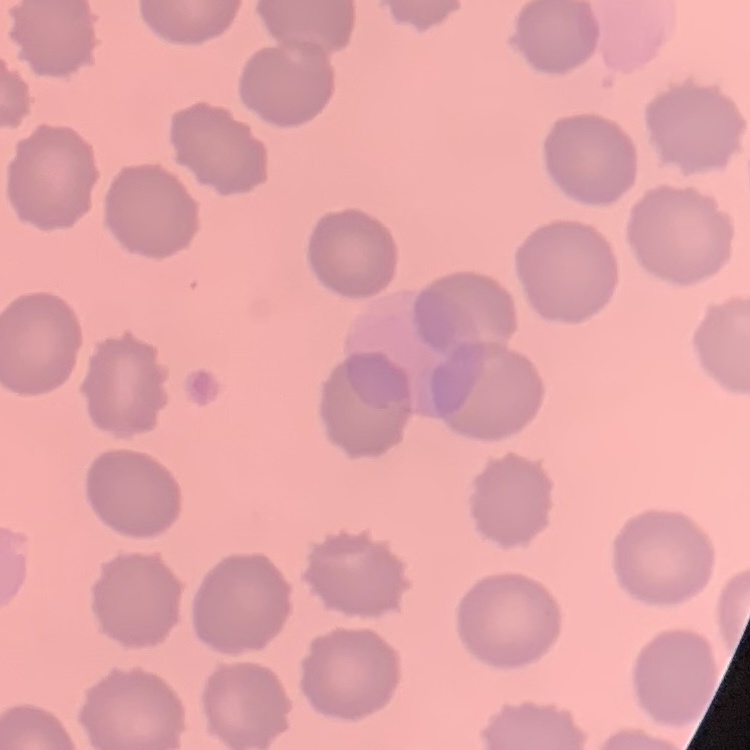 The red blood cells show no rouleaux formation. Field's or Giemsa stain. Thin blood smear. One tile cut from a larger photomicrograph.